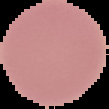

Summary:
  - Preparation: thin blood smear
  - Image size: 109×109 pixels
  - Image type: segmented cell region on a black background
  - Malaria status: uninfected